State which parasite is depicted.
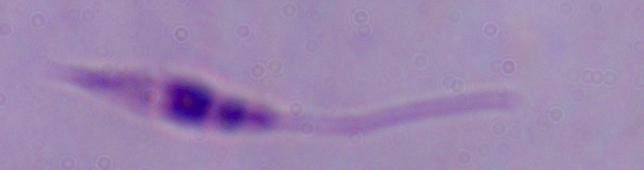
This is Leishmania.

1000x magnification. Micrograph.